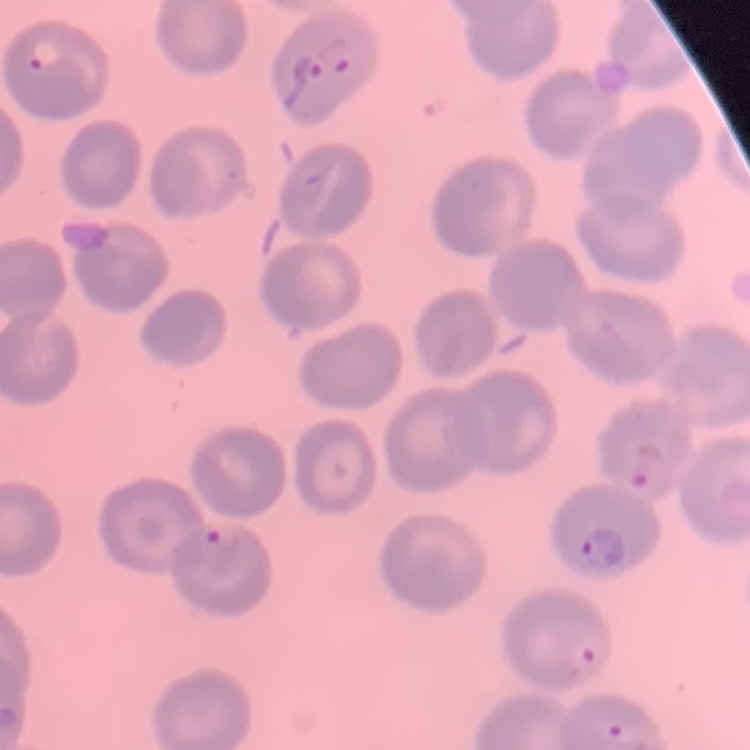
The red blood cells exhibit no rouleaux formation. Thin blood film. Square crop of a larger photomicrograph. Field's or Giemsa stain.